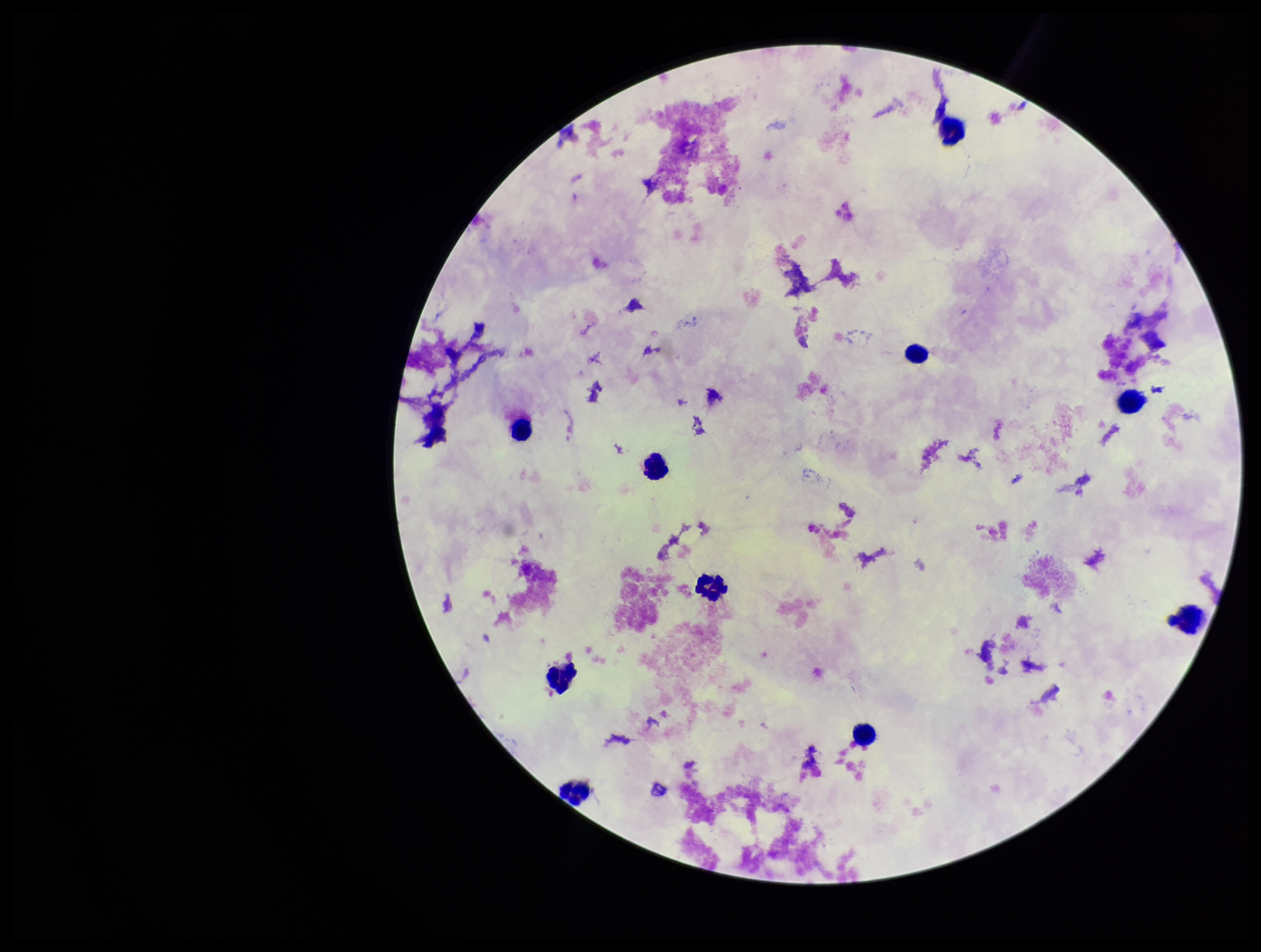

Image is 1261×952 pixels. Photographed through the microscope eyepiece with a smartphone camera. Preparation: thick. Stained with Giemsa. Plasmodium parasites: none seen. Patient malaria status: negative. Leukocyte count: 10. One field from this slide. Parasite count: 0.